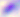

Summary:
  - Magnification: 400x
  - Modality: micrograph
  - Identification: Toxoplasma gondii